Name the cell type shown.
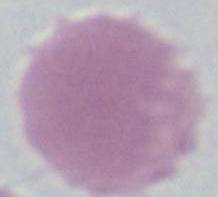

This is an erythrocyte.

Summary:
  - Magnification: 1000x
  - Modality: photomicrograph